Point out each Plasmodium parasite.
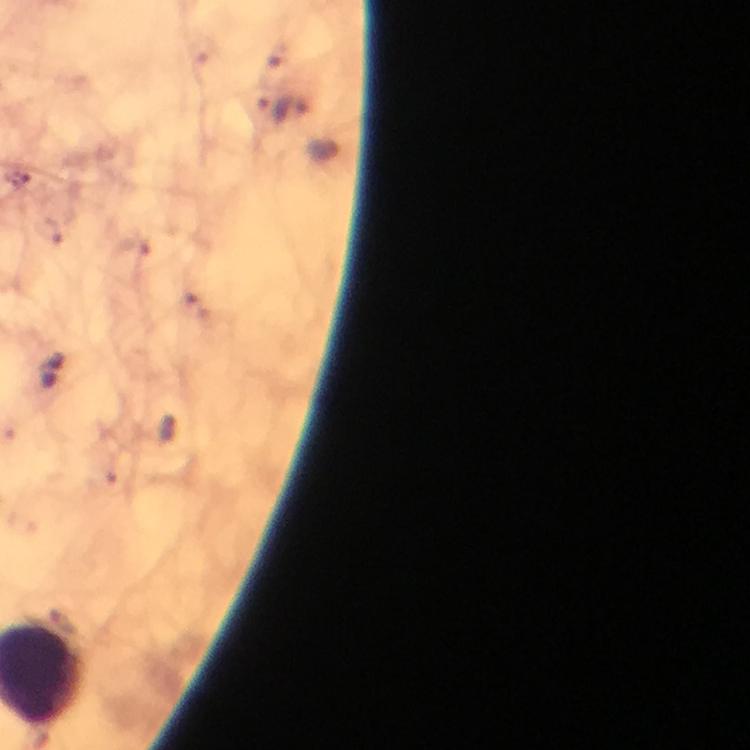
Approximate centers as (x, y) in pixels.
Plasmodium parasites: (272, 111).

immersion oil = applied
preparation = thick smear
stain = Giemsa
image size = 750×750 pixels
context = from a diagnostic examination for malaria
capture = smartphone camera through the microscope
magnification = 100x
cropped from = one field of view